State which cell type is depicted.
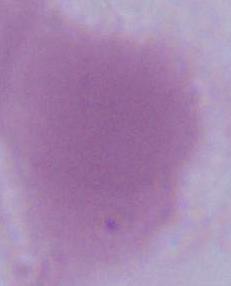

An erythrocyte.

modality = micrograph
magnification = 1000x